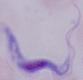

{
  "modality": "micrograph",
  "magnification": "1000x",
  "identification": "trypanosome"
}